Evaluate for malaria.
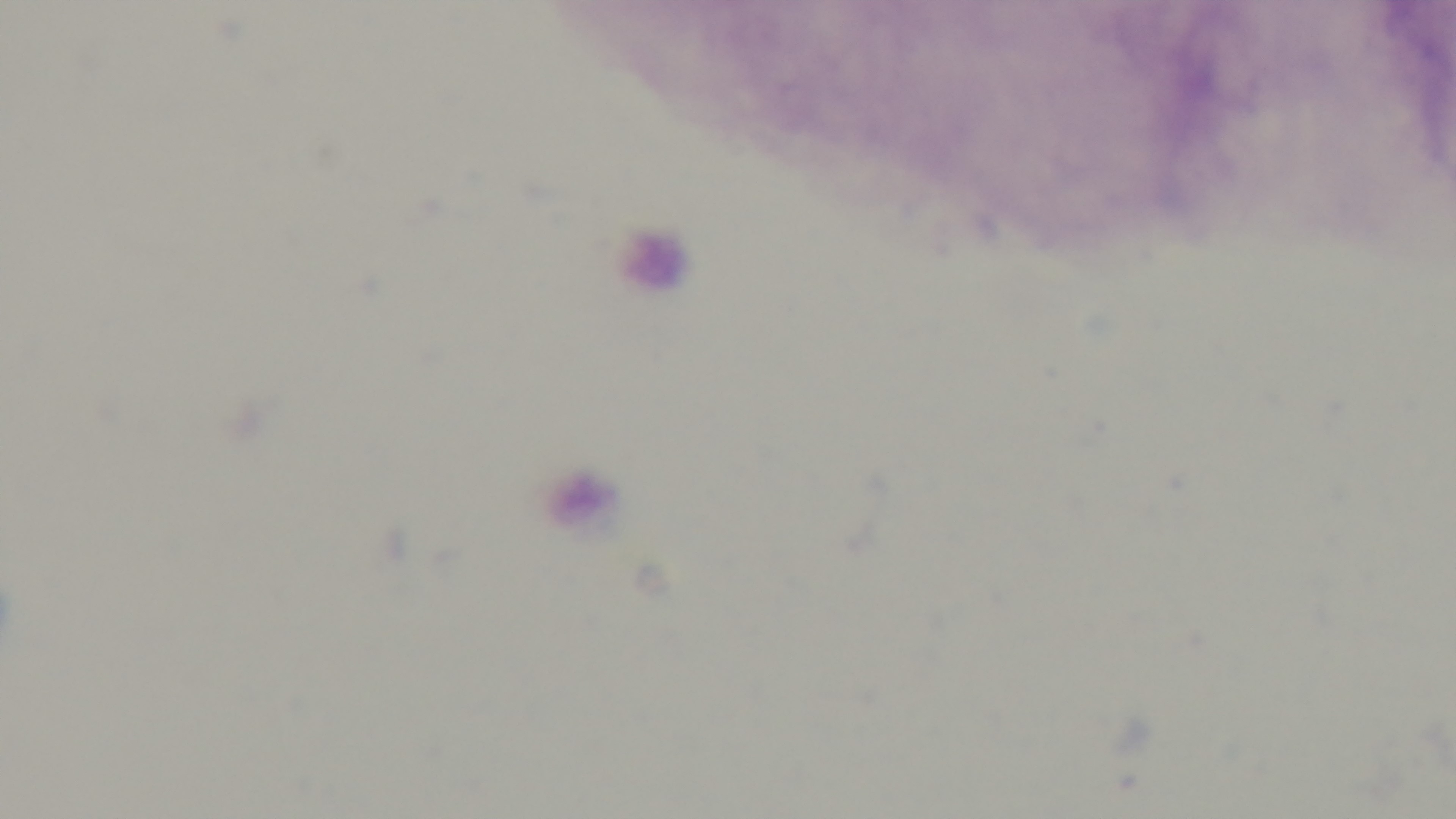
Uninfected.

Photomicrograph. Preparation: thick. Captured with a mounted 4K digital camera. Giemsa stain. One field from the slide. Oil-immersion objective, 100x.